Assess this cell for malaria.
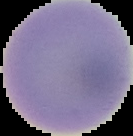
It is uninfected.

From a thin blood film. The area outside the segmented cell region is set to black. Image is 133×136 pixels.